Classify this cell by malaria status.
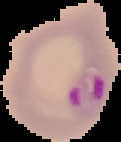

It is parasitized.

Summary:
  - Image type: segmented cell region on a black background
  - Image size: 121×142 pixels
  - Preparation: thin blood smear